Report the malaria status of this cell.
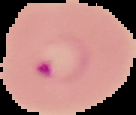

Parasitized.

Image is 136×115 pixels. Cell region segmented out of the field of view; the surrounding area is masked to black. From a thin blood smear.